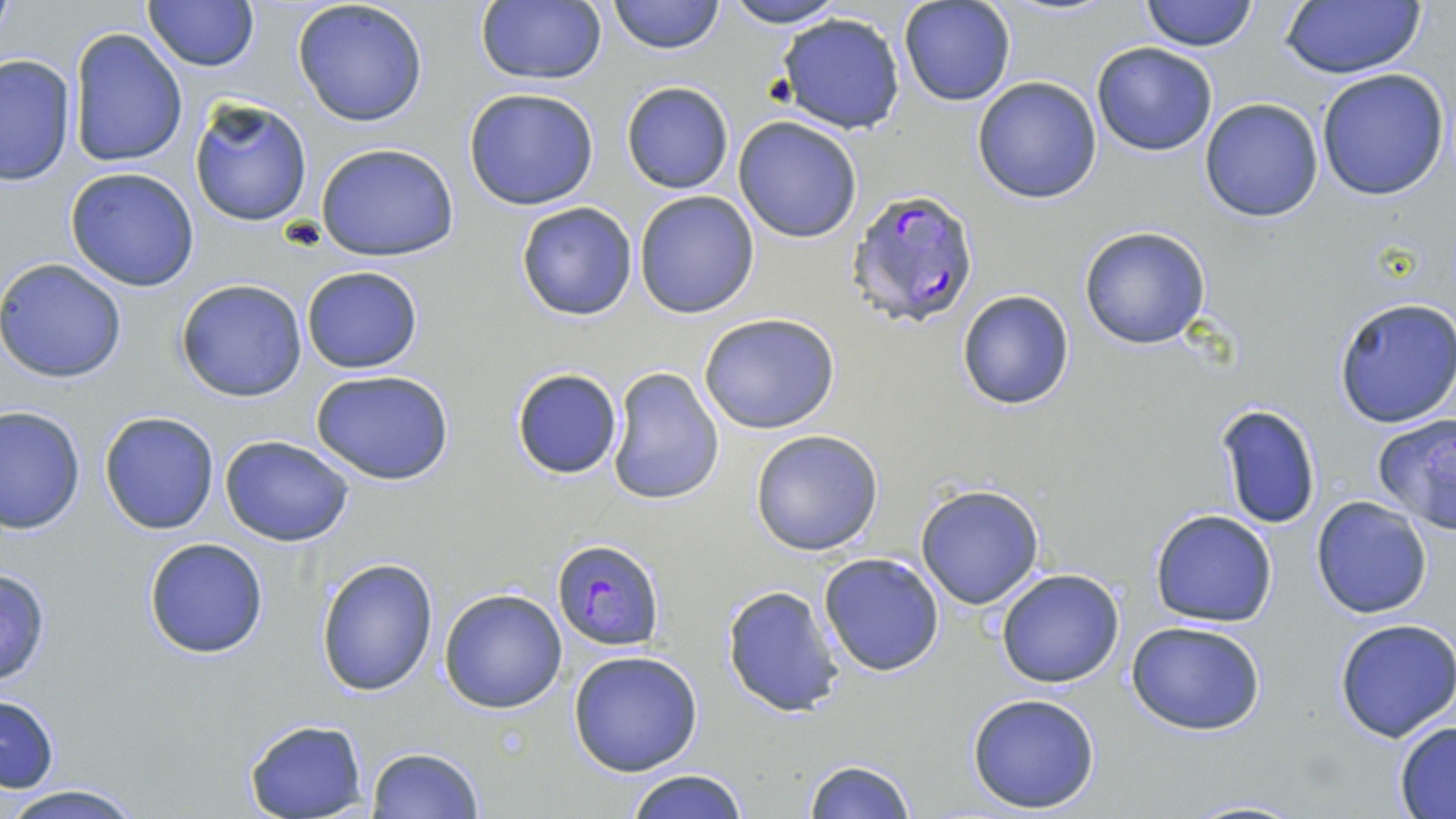
Summary:
  - Coordinate format: approximate bounding boxes as (x1,y1)-(x2,y2) corner pairs in pixels
  - Plasmodium falciparum-infected red blood cell locations: (847,188)-(981,330), (551,539)-(666,650)
  - Uninfected red blood cell locations: (142,0)-(257,71), (475,0)-(606,86), (607,0)-(724,55), (720,0)-(850,27), (1141,0)-(1258,50), (1279,0)-(1429,80), (291,1)-(429,128), (897,1)-(1016,106), (773,11)-(908,134), (68,28)-(188,169), (1090,42)-(1218,157), (0,55)-(76,187), (1315,68)-(1450,202), (972,76)-(1103,204), (620,81)-(734,195), (462,88)-(601,210), (189,95)-(314,228), (1199,97)-(1323,223), (733,115)-(863,242), (314,142)-(462,261), (65,166)-(200,291), (634,190)-(761,320), (516,201)-(638,321), (1079,226)-(1212,350), (0,258)-(128,384), (301,265)-(422,374), (176,278)-(308,402), (955,288)-(1075,411), (1331,296)-(1456,429), (698,312)-(841,434), (606,365)-(725,505), (510,367)-(624,480), (311,368)-(456,486), (1211,403)-(1323,531), (1,406)-(85,534), (99,411)-(219,535), (1371,414)-(1456,531), (750,429)-(885,557), (220,434)-(358,547), (914,482)-(1046,611), (1311,495)-(1432,618), (1149,509)-(1278,627), (143,537)-(271,659), (816,553)-(945,677), (315,557)-(439,697), (0,565)-(55,689), (995,568)-(1125,689), (721,585)-(846,717), (440,589)-(567,712), (1334,618)-(1456,741), (1126,620)-(1268,737), (568,649)-(704,776), (966,691)-(1102,813), (1,693)-(59,792), (243,719)-(367,818), (1392,720)-(1456,818), (365,746)-(485,818), (802,758)-(915,818), (626,767)-(750,819), (0,783)-(151,819), (1181,797)-(1310,818)
  - Slide-level diagnosis: Plasmodium falciparum
  - Preparation: thin blood smear
  - Stain: May-Grünwald-Giemsa
  - Field of view: single
  - Magnification: 1000x
  - Modality: light microscopy
  - Image size: 1456×819 pixels